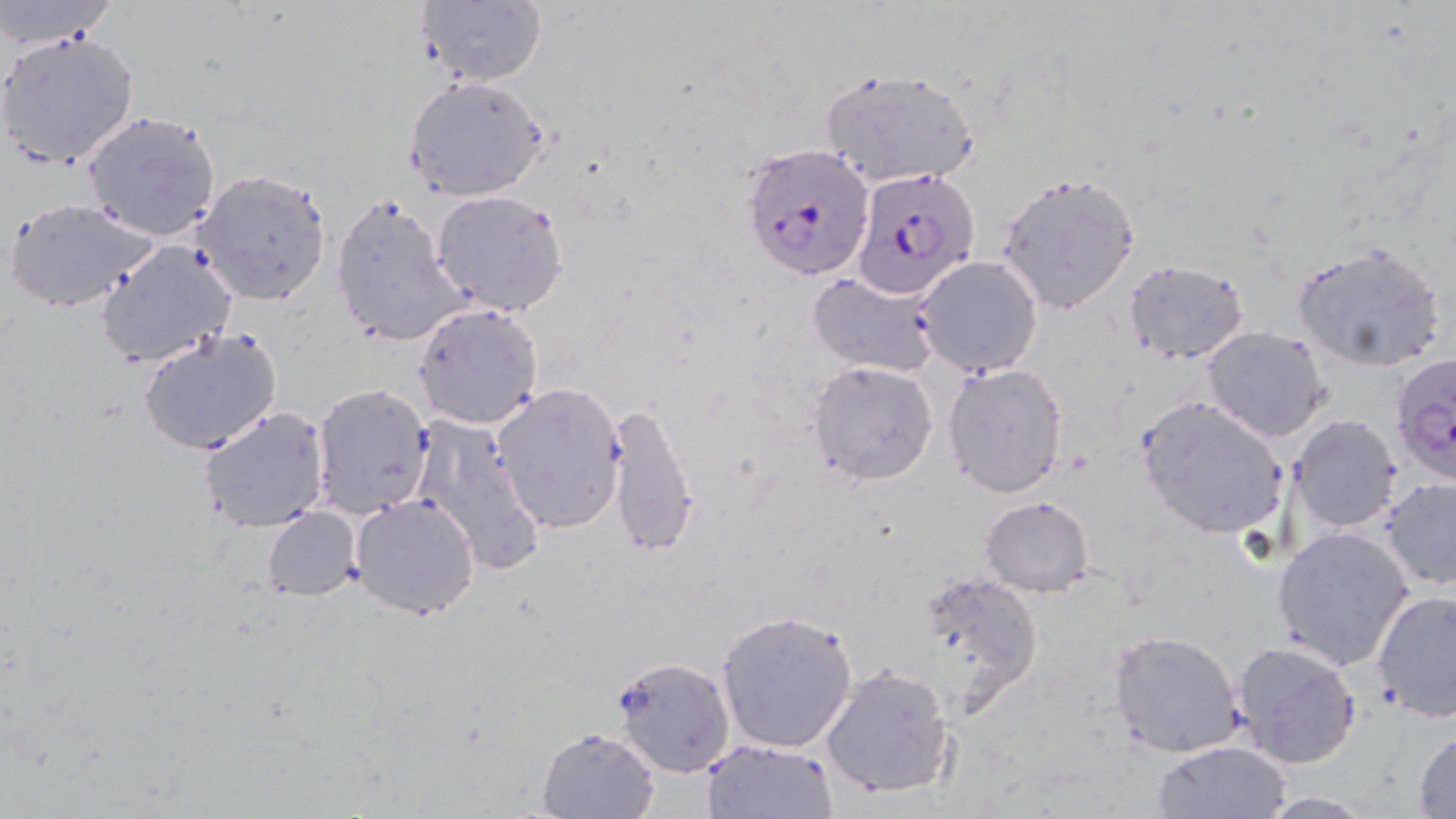
slide_level_diagnosis: Plasmodium falciparum
magnification: 1000x
image_size: 1456×819 pixels
modality: light microscopy
stain: May-Grünwald-Giemsa
uninfected_red_blood_cell_locations: 'approximate bounding boxes as [x1, y1, x2, y2] in pixels: [0, 0, 121, 49], [414, 1, 546, 88], [0, 30, 140, 170], [818, 65, 982, 191], [404, 76, 549, 201], [79, 110, 224, 244], [193, 169, 333, 306], [996, 171, 1140, 313], [430, 190, 569, 317], [330, 194, 465, 346], [7, 198, 157, 315], [98, 238, 240, 369], [1289, 241, 1450, 372], [916, 256, 1043, 377], [1122, 259, 1250, 364], [807, 271, 942, 378], [413, 302, 545, 431], [1201, 325, 1331, 441], [136, 326, 284, 459], [806, 359, 938, 487], [942, 362, 1070, 499], [310, 382, 434, 519], [493, 383, 626, 532], [1136, 394, 1290, 540], [602, 401, 700, 560], [199, 406, 331, 534], [410, 414, 547, 576], [1288, 414, 1404, 535], [1381, 477, 1456, 590], [350, 494, 481, 620], [979, 496, 1096, 596], [262, 506, 362, 601], [1270, 526, 1414, 671], [914, 571, 1043, 708], [1372, 590, 1456, 722], [715, 609, 859, 754], [1107, 629, 1244, 759], [1230, 640, 1362, 767], [610, 657, 733, 779], [820, 664, 956, 800], [536, 726, 661, 818], [1411, 731, 1456, 816], [700, 738, 839, 818], [1153, 741, 1292, 818], [1251, 792, 1381, 818]'
plasmodium_falciparum_infected_red_blood_cell_locations: 'approximate bounding boxes as [x1, y1, x2, y2] in pixels: [739, 141, 876, 281], [851, 168, 981, 297], [1389, 353, 1455, 488]'
field_of_view: single
preparation: thin blood smear